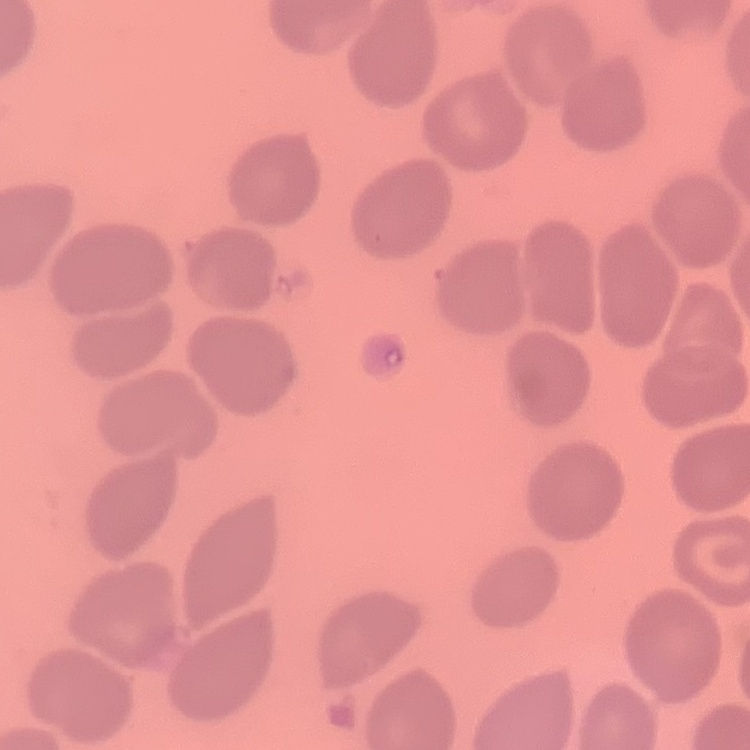

erythrocyte morphology = no rouleaux formation
stain = Field's or Giemsa
preparation = thin peripheral smear
image type = square crop of a larger photomicrograph